Identify the cell.
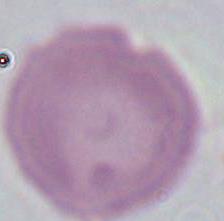

An erythrocyte.

1000x magnification. Photomicrograph.